Assess for Plasmodium parasites.
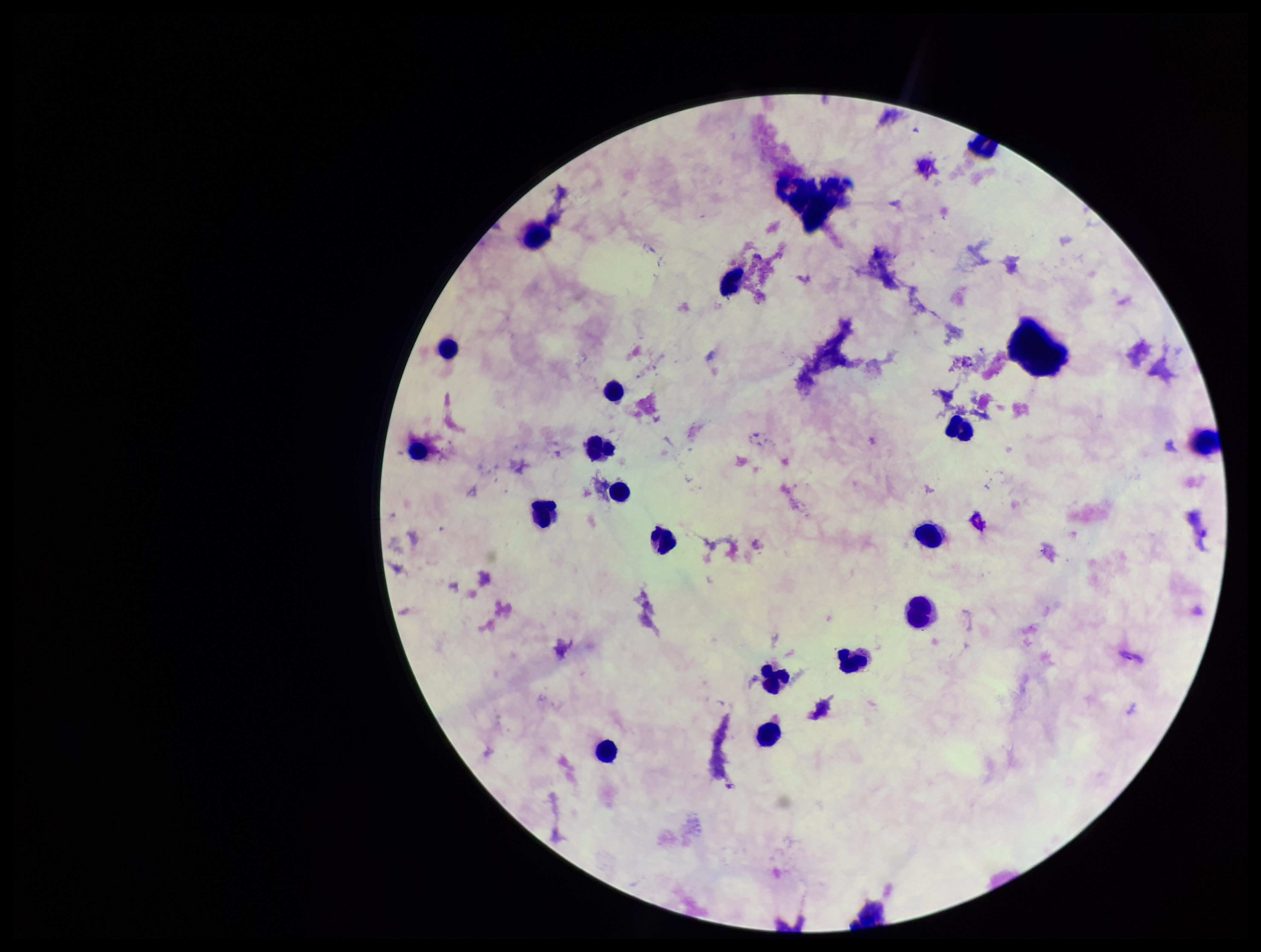
None detected.

Preparation: thick smear. Giemsa stain. Parasite count: 0. Leukocyte count: 19. Single field of view. Image is 1261×952 pixels. Smartphone photograph taken through the eyepiece of a microscope. Patient malaria status: negative.